Assess this cell for malaria.
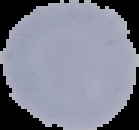
It is uninfected.

Summary:
  - Image type: cell region segmented out of the field of view; surrounding area masked to black
  - Image size: 139×130 pixels
  - Preparation: thin blood film